Assess this cell for malaria.
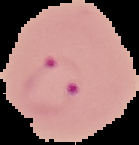

It is parasitized.

Summary:
  - Image type: segmented cell region on a black background
  - Image size: 139×145 pixels
  - Preparation: thin blood smear